Comment on the morphology of the red blood cells.
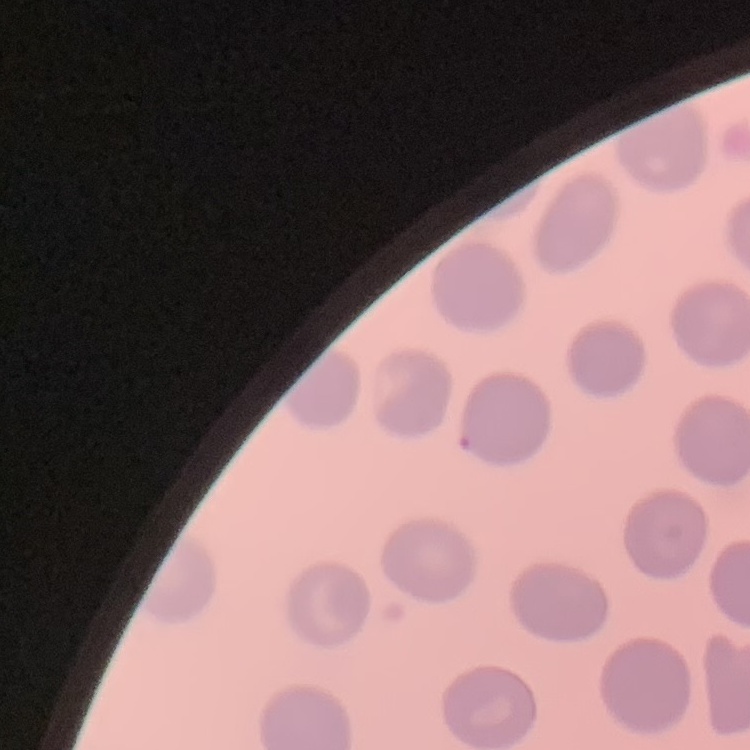
No rouleaux formation.

image type = one tile cut from a larger photomicrograph
preparation = thin blood film
stain = Field's or Giemsa